Name the blood parasite species.
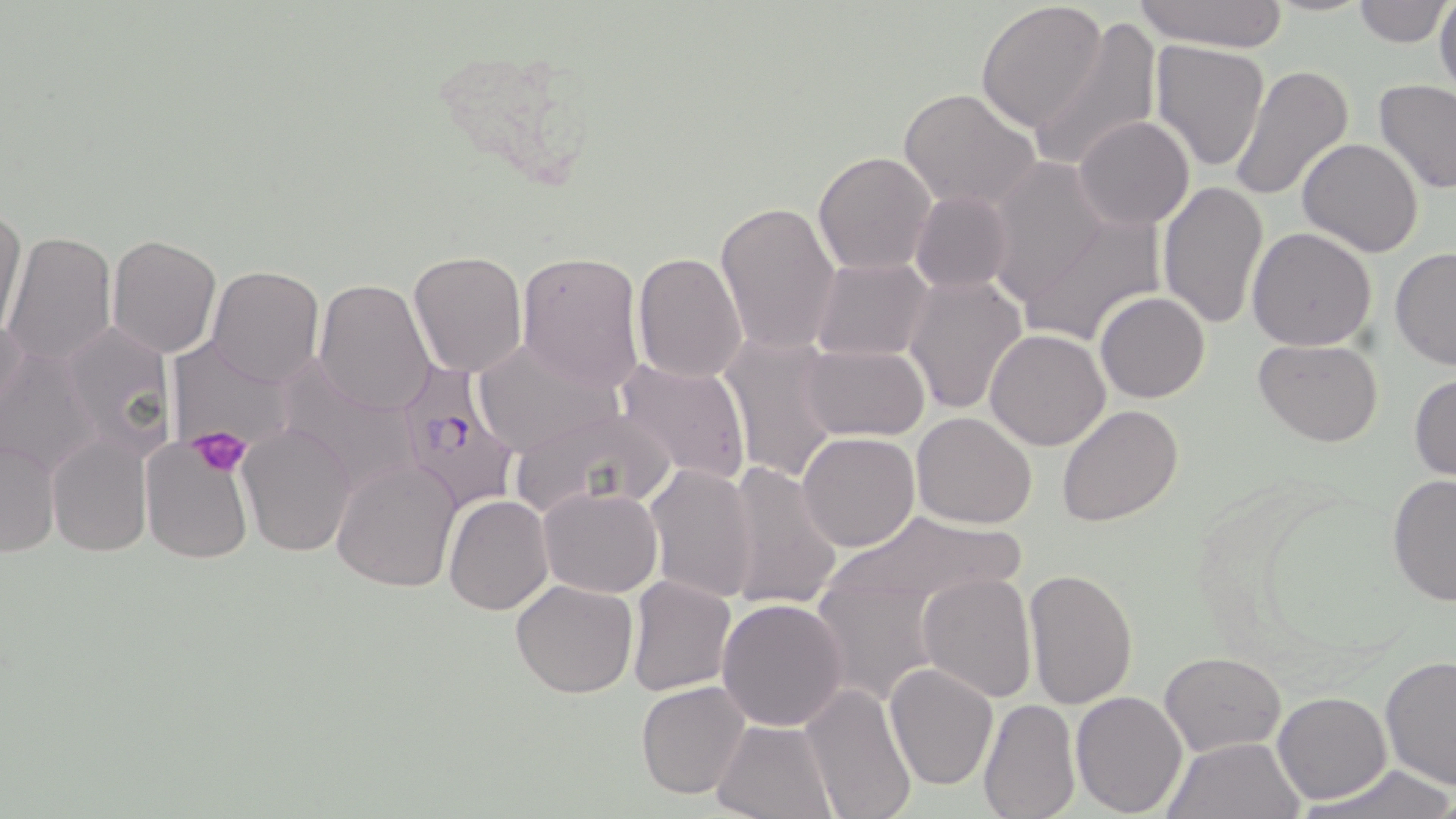
Plasmodium falciparum.

Approximate bounding boxes as (x1,y1)-(x2,y2) corner pairs in pixels. Uninfected red blood cell locations: (1129,0)-(1292,51), (1352,0)-(1450,46), (1433,0)-(1456,101), (975,2)-(1108,133), (1414,3)-(1455,82), (1029,16)-(1162,175), (1149,41)-(1271,171), (1229,65)-(1353,202), (1375,79)-(1456,195), (898,89)-(1042,212), (1074,117)-(1194,229), (1297,138)-(1423,257), (813,150)-(937,276), (984,160)-(1109,309), (1157,179)-(1268,328), (910,189)-(1012,295), (715,200)-(842,354), (0,204)-(28,342), (1016,211)-(1167,349), (1247,228)-(1378,351), (3,232)-(117,368), (107,234)-(224,357), (1389,247)-(1456,372), (407,250)-(529,376), (515,250)-(646,393), (631,252)-(749,384), (811,256)-(932,362), (206,265)-(325,386), (904,273)-(1028,416), (313,279)-(436,416), (1094,292)-(1210,404), (0,310)-(29,433), (62,323)-(172,459), (986,327)-(1111,449), (719,333)-(842,483), (469,337)-(623,459), (1253,338)-(1385,448), (0,339)-(102,479), (165,340)-(308,446), (798,344)-(929,441), (613,356)-(752,487), (295,360)-(432,483), (1410,372)-(1456,481), (509,405)-(678,519), (1058,405)-(1184,527), (912,412)-(1038,529), (239,422)-(355,556), (797,431)-(922,552), (2,434)-(60,560), (47,434)-(152,558), (140,441)-(254,566), (331,458)-(460,593), (724,460)-(841,612), (645,463)-(759,603), (1385,476)-(1456,606), (539,486)-(661,597), (444,495)-(554,616), (817,507)-(1027,616), (1023,568)-(1138,710), (918,572)-(1037,703), (626,576)-(736,696), (815,577)-(936,705), (511,580)-(639,698), (716,598)-(849,731), (1160,652)-(1284,756), (1379,656)-(1456,788), (884,662)-(998,791), (636,681)-(751,800), (799,682)-(917,819), (1070,691)-(1188,817), (1273,691)-(1392,804), (978,698)-(1078,819), (713,719)-(838,819), (1162,735)-(1304,819), (1302,765)-(1456,819). Plasmodium falciparum-infected red blood cell locations: (390,364)-(521,516). Platelet locations: (189,425)-(252,479). 1000x magnification. Light microscopy. Single field of view. May-Grünwald-Giemsa stain. Thin blood smear. Image is 1456×819 pixels.